Report the malaria status of this cell.
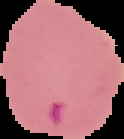
Parasitized.

Summary:
  - Preparation: thin blood smear
  - Image type: segmented cell region with the area outside set to black
  - Image size: 124×139 pixels